Point out each malaria parasite and each leukocyte.
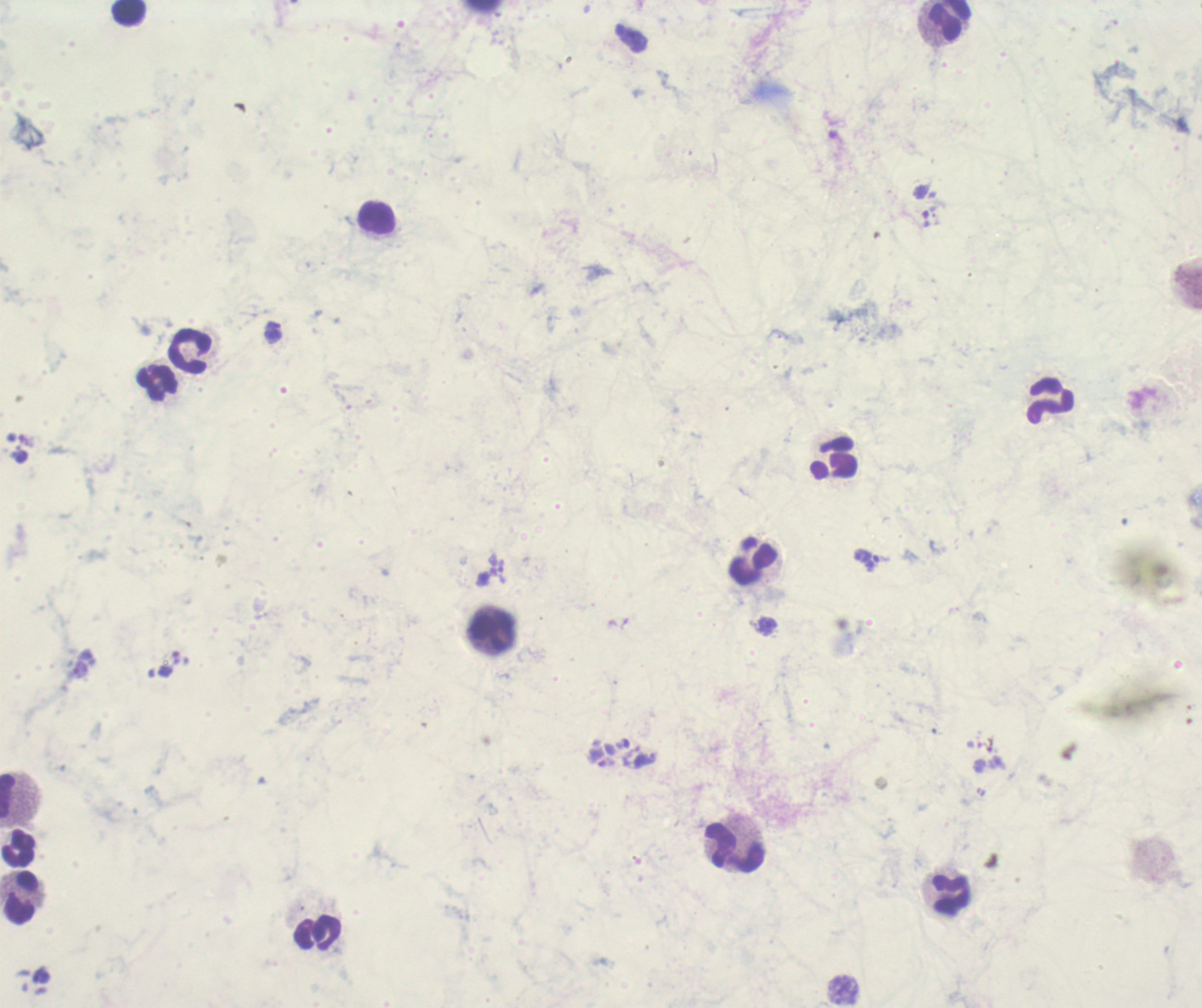
Approximate centers as [x, y] in pixels.
Trophozoites: [871, 562], [767, 626].
No schizont or gametocyte forms observed.
Leukocytes: [129, 14], [945, 20], [375, 218], [189, 353], [157, 383], [1050, 401], [836, 457], [754, 561], [490, 629], [8, 794], [734, 847], [18, 849], [950, 895], [21, 898], [316, 933].

Summary:
  - Image size: 1202×1008 pixels
  - Stain: Romanowsky
  - Field of view: single
  - Preparation: thick blood film
  - Background quality: poor
  - Magnification: 100x
  - Coloration quality: bad
  - Context: previously used in an actual diagnosis